Assess this cell for malaria.
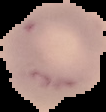
It is uninfected.

Summary:
  - Image size: 106×112 pixels
  - Image type: cell region segmented out of the field of view; surrounding area masked to black
  - Preparation: thin blood film